Describe the morphology of the erythrocytes.
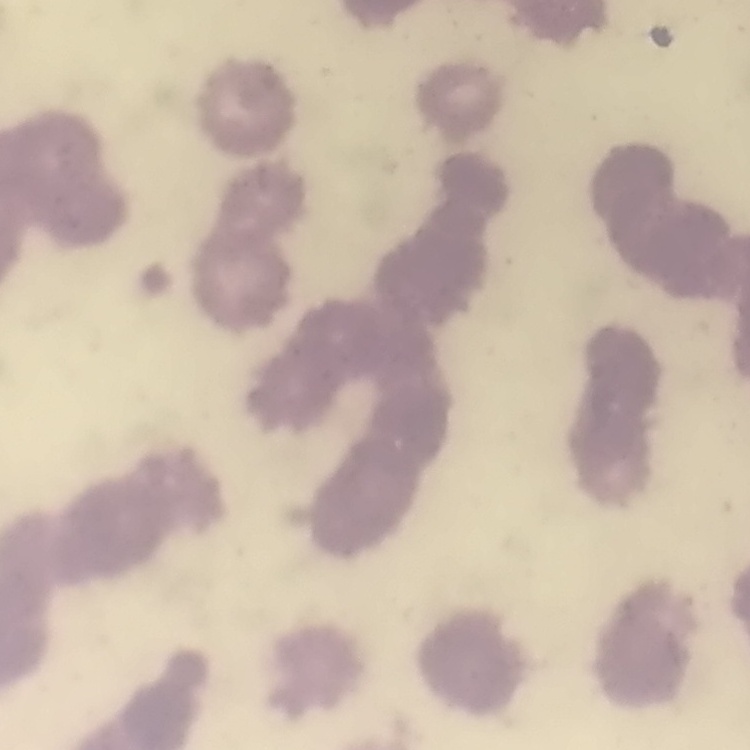

They show rouleaux formation.

Stained with either Field's or Giemsa. One tile cut from a larger photomicrograph. Thin peripheral smear.